Classify this cell by malaria status.
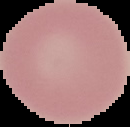

Uninfected.

Summary:
  - Image type: segmented cell region with the area outside set to black
  - Image size: 130×127 pixels
  - Preparation: thin blood film